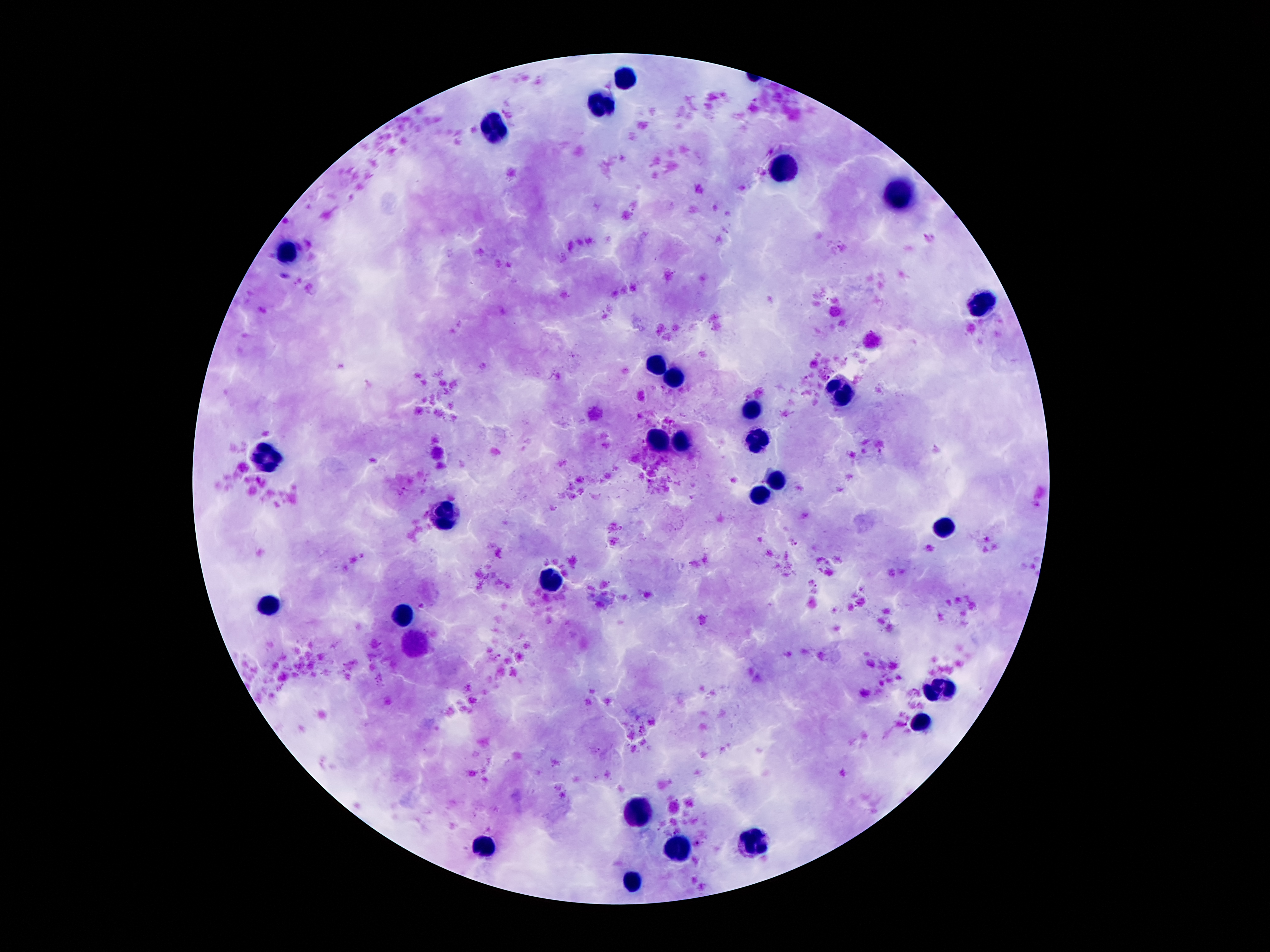

Approximate object centers, in pixels from the top-left corner.
Summary:
  - Plasmodium parasite locations: (x=828, y=376), (x=746, y=396), (x=793, y=543), (x=816, y=587), (x=676, y=831), (x=698, y=844)
  - Leukocyte locations: (x=625, y=78), (x=600, y=108), (x=499, y=131), (x=785, y=174), (x=903, y=196), (x=289, y=249), (x=987, y=300), (x=656, y=367), (x=676, y=378), (x=841, y=394), (x=751, y=409), (x=681, y=439), (x=757, y=439), (x=659, y=441), (x=273, y=456), (x=774, y=481), (x=763, y=493), (x=446, y=515), (x=945, y=526), (x=547, y=579), (x=270, y=604), (x=404, y=615), (x=412, y=643), (x=939, y=691), (x=920, y=722), (x=637, y=814), (x=757, y=845), (x=483, y=851), (x=679, y=854), (x=631, y=884)
  - Preparation: thick blood film
  - Field of view: single
  - Magnification: 100x
  - Patient malaria status: positive for Plasmodium falciparum
  - Stain: Giemsa
  - Image size: 1270×952 pixels
  - Capture: smartphone camera through the microscope eyepiece